Outline each blood parasite and name the species.
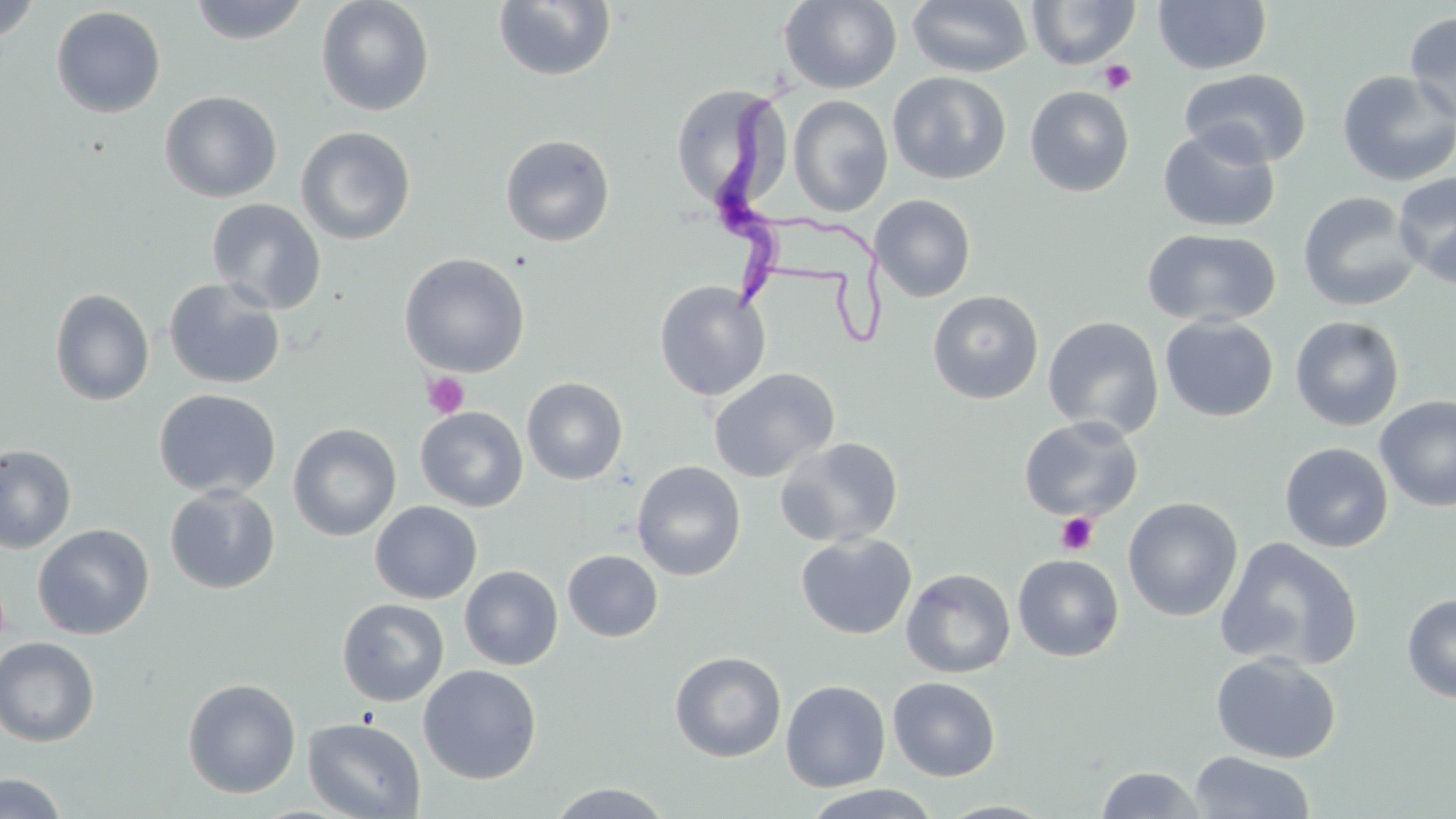

Approximate bounding boxes as [x1, y1, x2, y2] in pixels.
Trypanosoma brucei: [712, 63, 803, 316].
No Plasmodium falciparum, Plasmodium ovale, Plasmodium malariae, Plasmodium vivax, or Babesia divergens observed.

Summary:
  - Uninfected red blood cell locations: [187, 0, 312, 45], [315, 0, 435, 116], [492, 0, 616, 82], [779, 0, 902, 94], [906, 0, 1033, 78], [1026, 0, 1141, 69], [1152, 0, 1272, 75], [0, 1, 43, 44], [51, 6, 166, 118], [1404, 11, 1456, 126], [1179, 68, 1312, 167], [1335, 70, 1456, 188], [887, 71, 1012, 185], [671, 83, 788, 211], [1024, 86, 1135, 197], [159, 90, 283, 203], [788, 95, 893, 216], [1157, 125, 1281, 233], [295, 126, 416, 246], [500, 133, 616, 247], [1393, 171, 1456, 288], [1297, 191, 1422, 312], [870, 194, 976, 302], [206, 198, 326, 314], [1141, 228, 1281, 328], [399, 252, 530, 377], [163, 277, 286, 389], [653, 280, 772, 402], [49, 288, 155, 406], [927, 289, 1044, 404], [1159, 315, 1279, 422], [1043, 316, 1164, 439], [1289, 316, 1405, 432], [708, 368, 840, 483], [521, 377, 629, 485], [153, 388, 281, 498], [1374, 395, 1456, 513], [415, 406, 528, 512], [1018, 415, 1144, 522], [287, 423, 401, 541], [774, 436, 904, 548], [1279, 442, 1393, 553], [0, 443, 77, 554], [631, 460, 746, 581], [165, 485, 281, 595], [1122, 496, 1243, 621], [370, 500, 483, 604], [32, 523, 155, 640], [795, 533, 917, 639], [1215, 536, 1363, 672], [563, 550, 664, 642], [1012, 553, 1125, 661], [459, 565, 563, 670], [901, 568, 1016, 678], [1401, 593, 1456, 703], [337, 598, 449, 706], [0, 637, 100, 746], [669, 651, 787, 762], [1210, 652, 1342, 764], [418, 664, 542, 784], [888, 677, 1000, 781], [182, 678, 301, 798], [780, 679, 891, 792], [303, 717, 426, 818], [1188, 750, 1316, 818], [1095, 766, 1206, 819], [0, 772, 69, 818], [544, 782, 676, 818], [798, 784, 946, 818], [934, 800, 1058, 819]
  - Platelet locations: [1099, 60, 1137, 94], [422, 372, 470, 418], [1055, 511, 1098, 555]
  - Slide-level diagnosis: Trypanosoma brucei
  - Modality: light microscopy
  - Stain: May-Grünwald-Giemsa
  - Magnification: 1000x
  - Field of view: single
  - Image size: 1456×819 pixels
  - Preparation: thin blood film